Give the position of every Plasmodium parasite.
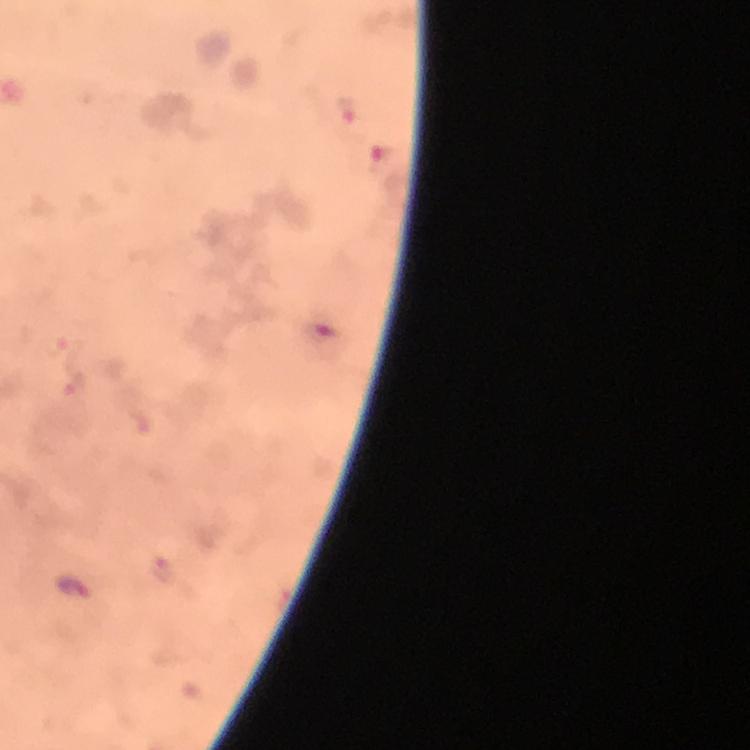

Approximate centers as [x, y] in pixels.
Plasmodium parasites: [75, 587].

Image is 750×750 pixels. Thick blood film. From a diagnostic examination for malaria. Cropped region of a single field of view. At 100x magnification. Immersion oil applied. Giemsa-stained preparation. Smartphone photograph taken through a microscope.